State the blood parasite species.
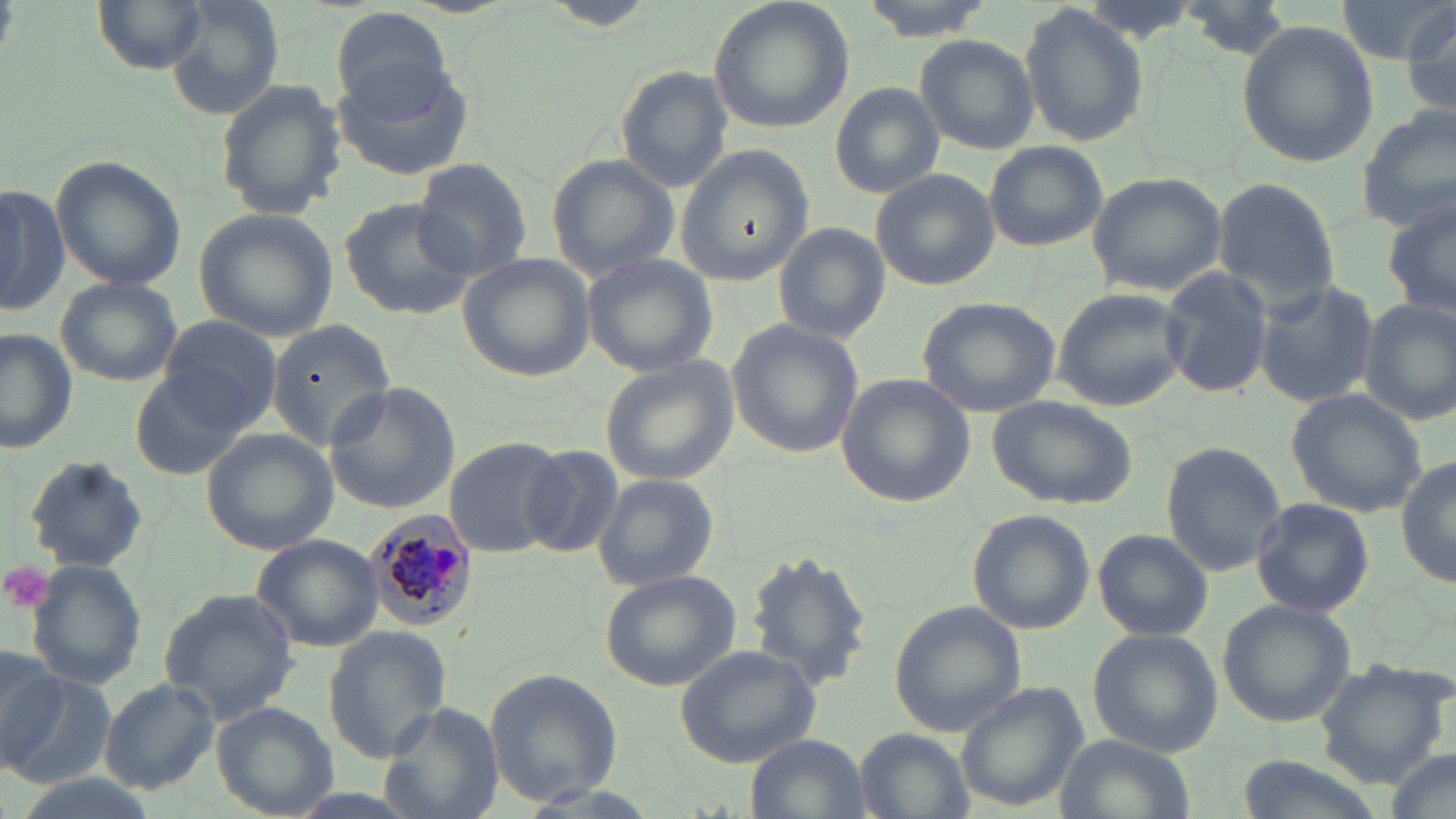

Plasmodium malariae.

uninfected_red_blood_cell_locations: 'approximate bounding boxes as (x1, y1, x2, y2) in pixels: (91, 0, 211, 72), (163, 0, 284, 119), (706, 0, 855, 138), (857, 0, 994, 40), (1337, 0, 1452, 65), (537, 1, 662, 32), (1398, 4, 1456, 120), (1022, 5, 1147, 147), (331, 6, 453, 116), (1237, 22, 1378, 167), (914, 33, 1036, 154), (330, 60, 478, 181), (614, 66, 735, 191), (215, 79, 345, 221), (830, 82, 945, 198), (1357, 106, 1455, 233), (984, 141, 1108, 252), (674, 146, 814, 288), (545, 154, 678, 280), (49, 155, 187, 291), (410, 158, 533, 280), (871, 170, 999, 291), (1088, 172, 1229, 297), (1210, 176, 1343, 303), (0, 182, 68, 319), (338, 196, 475, 321), (1385, 197, 1456, 323), (193, 207, 338, 341), (772, 222, 888, 344), (582, 252, 721, 377), (458, 253, 594, 383), (1160, 267, 1275, 400), (54, 277, 182, 387), (1253, 281, 1379, 407), (1052, 286, 1184, 410), (917, 296, 1063, 419), (1360, 299, 1456, 426), (155, 316, 285, 435), (267, 318, 399, 452), (726, 319, 863, 458), (0, 328, 77, 454), (600, 357, 738, 484), (131, 366, 259, 481), (835, 374, 975, 506), (324, 381, 460, 514), (1287, 388, 1429, 517), (989, 394, 1138, 510), (202, 431, 336, 554), (443, 436, 567, 556), (1161, 441, 1287, 576), (518, 443, 622, 558), (23, 455, 148, 574), (1396, 458, 1456, 589), (591, 472, 721, 591), (1250, 497, 1376, 618), (967, 509, 1095, 635), (1094, 530, 1212, 640), (249, 535, 383, 651), (742, 549, 877, 692), (27, 560, 148, 692), (600, 571, 740, 693), (158, 588, 301, 723), (1217, 601, 1356, 728), (888, 602, 1025, 738), (322, 628, 452, 762), (1086, 629, 1221, 756), (673, 644, 821, 769), (0, 647, 65, 773), (1310, 658, 1451, 790), (485, 668, 622, 806), (3, 670, 115, 789), (99, 680, 220, 795), (952, 684, 1090, 815), (212, 701, 342, 819), (383, 705, 505, 819), (856, 730, 972, 819), (745, 733, 869, 818), (1054, 734, 1195, 819), (1381, 750, 1455, 819)'
modality: optical microscopy
platelet_locations: 'approximate bounding boxes as (x1, y1, x2, y2) in pixels: (1, 562, 55, 619)'
stain: May-Grünwald-Giemsa
image_size: 1456×819 pixels
magnification: 1000x
plasmodium_malariae_infected_red_blood_cell_locations: 'approximate bounding boxes as (x1, y1, x2, y2) in pixels: (365, 507, 477, 637)'
preparation: thin blood film
field_of_view: one of a larger specimen